Report the malaria status of this cell.
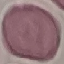
It is uninfected.

Giemsa stain. Cell patch, automatically extracted from a larger field of view and resized to 64 × 64 pixels. Thin blood smear. Photographed with a smartphone camera at the microscope eyepiece.